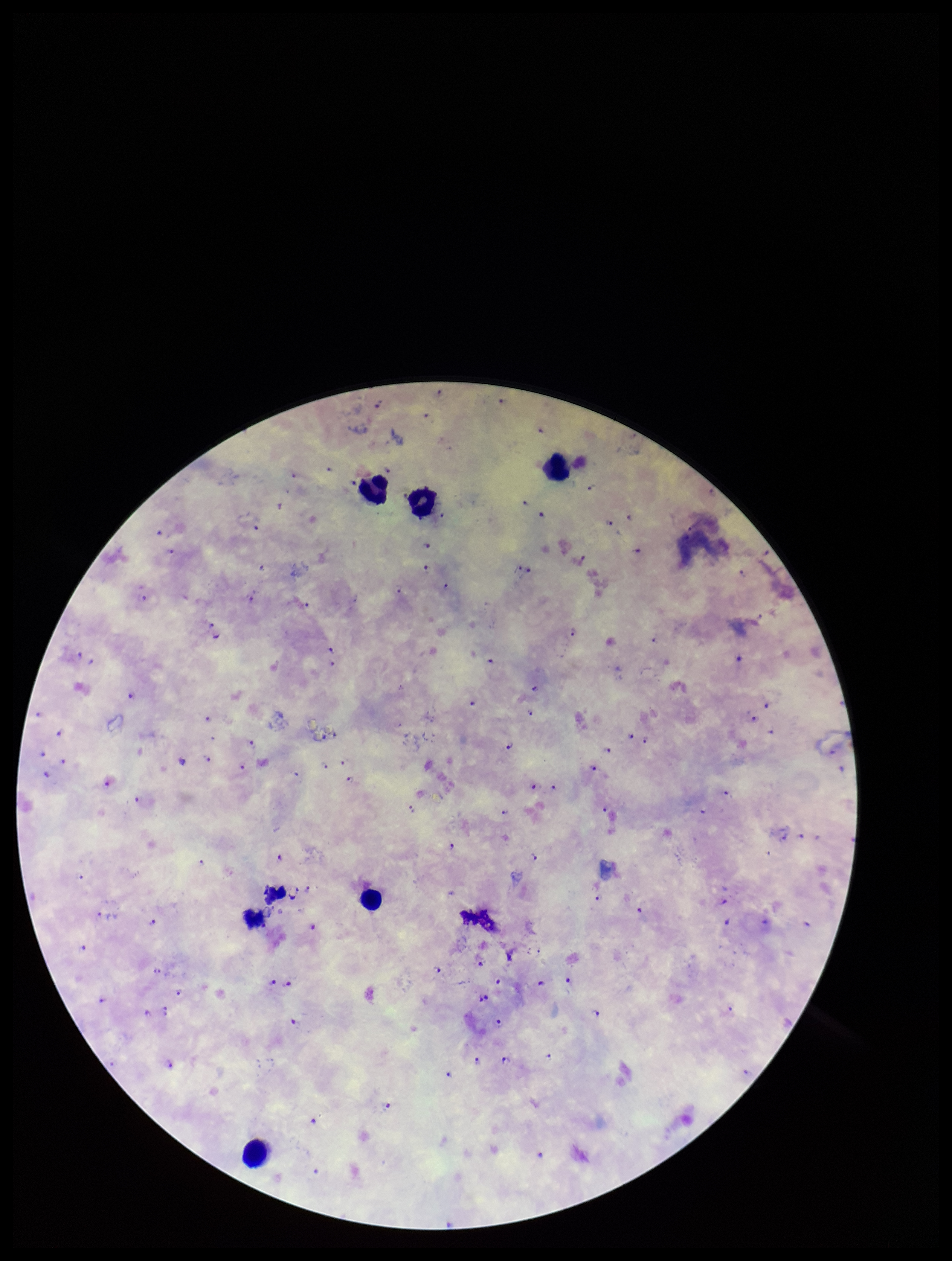 Patient malaria status: positive. Image is 952×1261 pixels. Leukocyte count: 6. Preparation: thick. Plasmodium parasites: detected. Smartphone photograph taken through the eyepiece of a microscope. Giemsa stain. Species reported for this patient: Plasmodium falciparum. Parasite count: 110. Single field of view.